Give the position of every malaria parasite and every leukocyte.
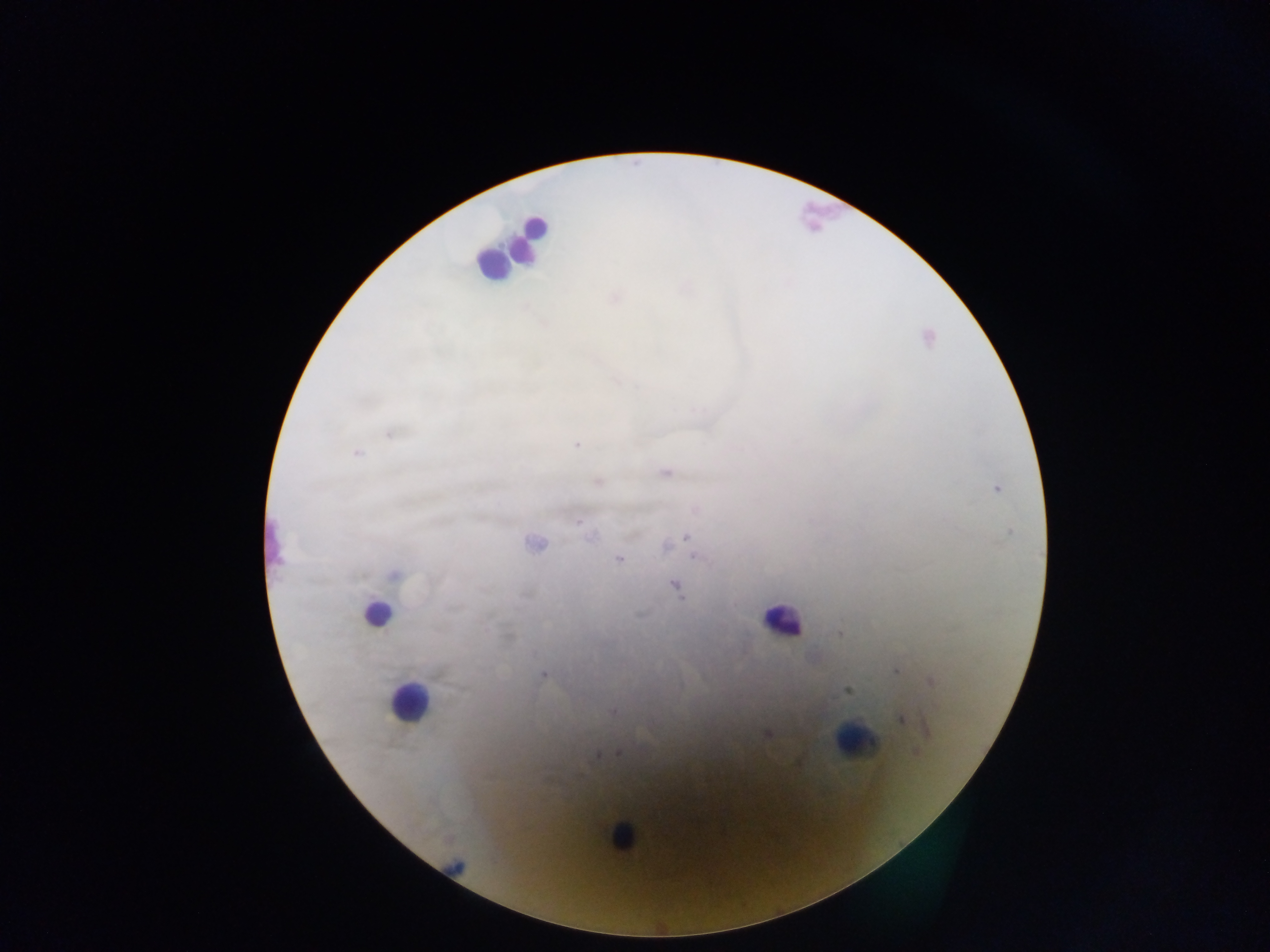

Approximate centers as x y in pixels.
Malaria parasites: 614 298; 390 434; 576 444; 357 452; 665 472; 598 482; 996 489; 696 509; 578 522; 591 536; 686 537; 534 544; 666 547; 696 557; 619 559; 674 587; 838 634; 895 670; 542 674; 931 682; 846 690; 613 712; 900 719; 928 730; 767 734; 618 753; 597 754.
Leukocytes: 528 237; 491 263; 270 543; 376 613; 782 620; 408 702; 854 741; 621 836.

country: Ghana
preparation: thick blood film
capture: mobile-phone photograph through a microscope
image_size: 1270×952 pixels
field_of_view: single